Describe the morphology of the erythrocytes.
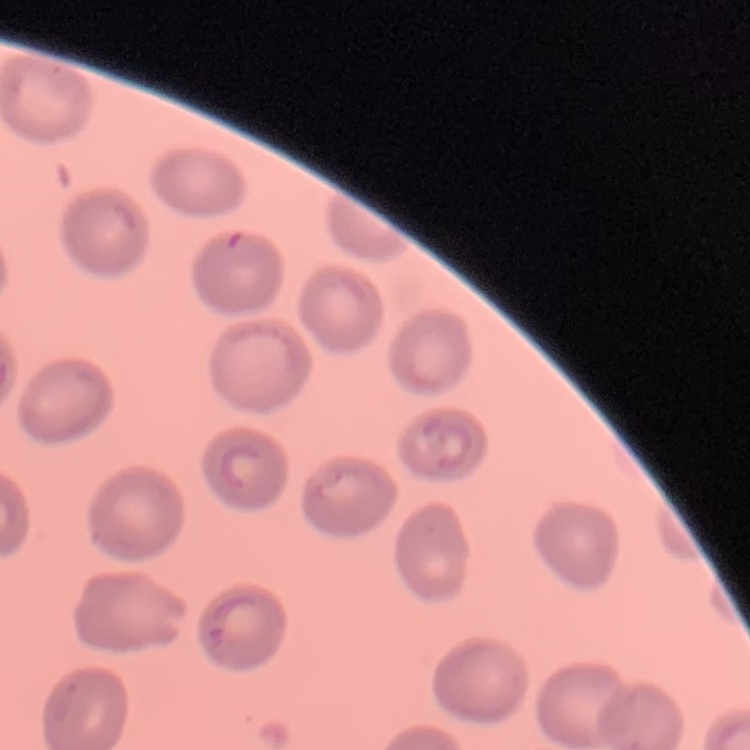
No rouleaux formation.

Thin blood film. Stained with either Field's or Giemsa. One tile cut from a larger photomicrograph.